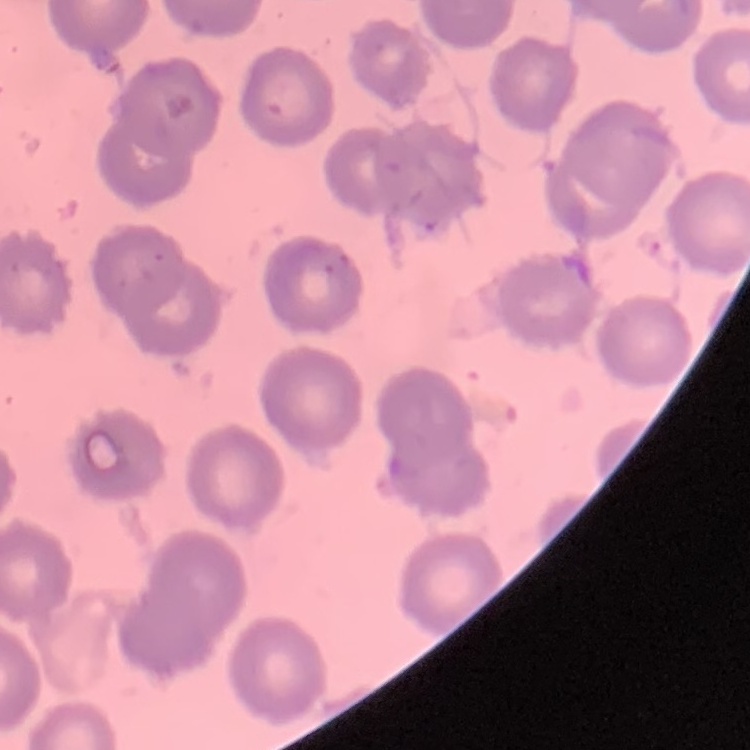

{
  "red_blood_cell_morphology": "no rouleaux formation",
  "image_type": "square crop of a larger photomicrograph",
  "preparation": "thin peripheral smear",
  "stain": "Field's or Giemsa"
}